Assess this cell for malaria.
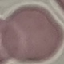
Uninfected.

Summary:
  - Image type: automatically extracted cell patch, resized to 64 × 64 pixels
  - Capture: smartphone through the microscope eyepiece
  - Preparation: thin smear
  - Stain: Giemsa